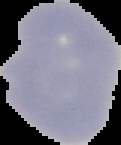 Result: negative for malaria parasites. Cell region segmented out of the field of view; the surrounding area is masked to black. From a thin blood smear. Image is 121×145 pixels.